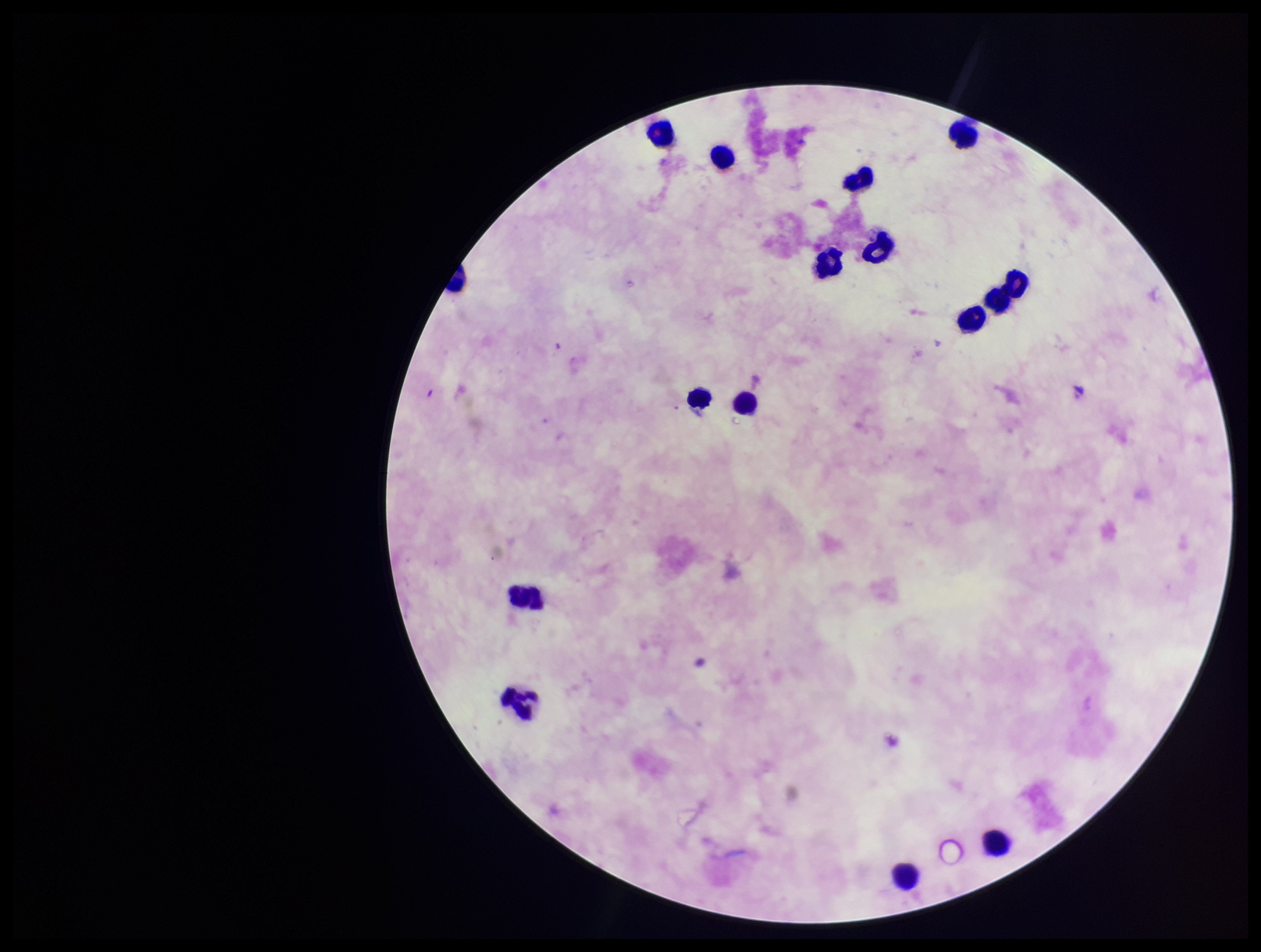

image size = 1261×952 pixels
capture = smartphone photograph through the microscope eyepiece
field of view = one from this slide
parasite count = 0
stain = Giemsa
Plasmodium parasites = none detected
patient malaria status = negative
leukocyte count = 16
preparation = thick smear